Identify the parasite.
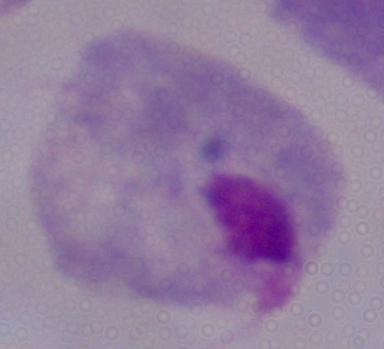
This is a trichomonad.

Summary:
  - Magnification: 1000x
  - Modality: micrograph